Report the malaria status of this cell.
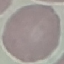

It is uninfected.

Summary:
  - Stain: Giemsa
  - Preparation: thin blood film
  - Capture: smartphone camera at the microscope eyepiece
  - Image type: automatically extracted cell patch, resized to 64 × 64 pixels